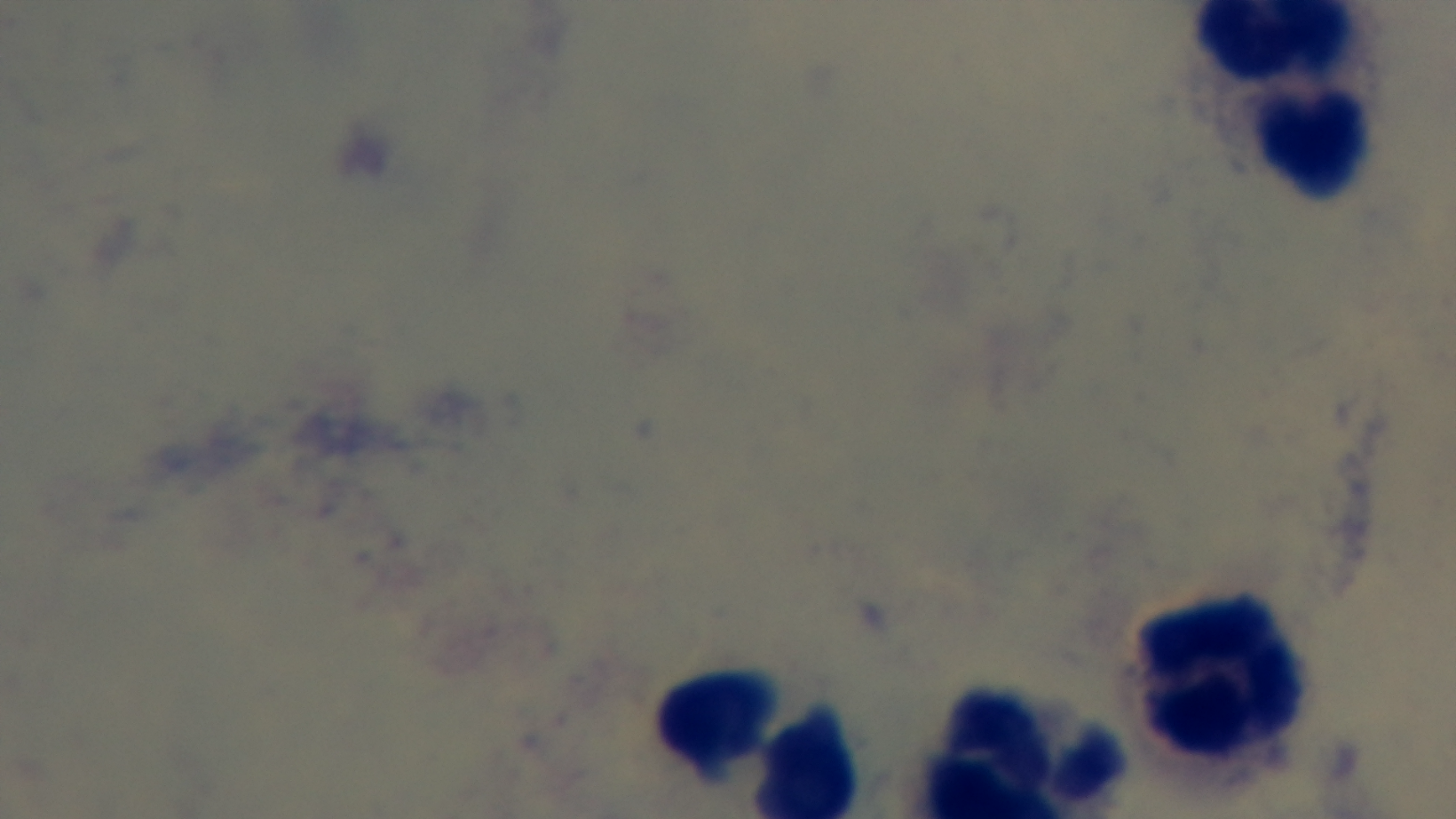
{
  "objective": "100x oil immersion",
  "malaria_status": "negative",
  "capture": "mounted 4K digital camera",
  "preparation": "thick smear",
  "field_of_view": "one from the slide",
  "stain": "Giemsa",
  "modality": "light microscopy"
}